State the preparation type.
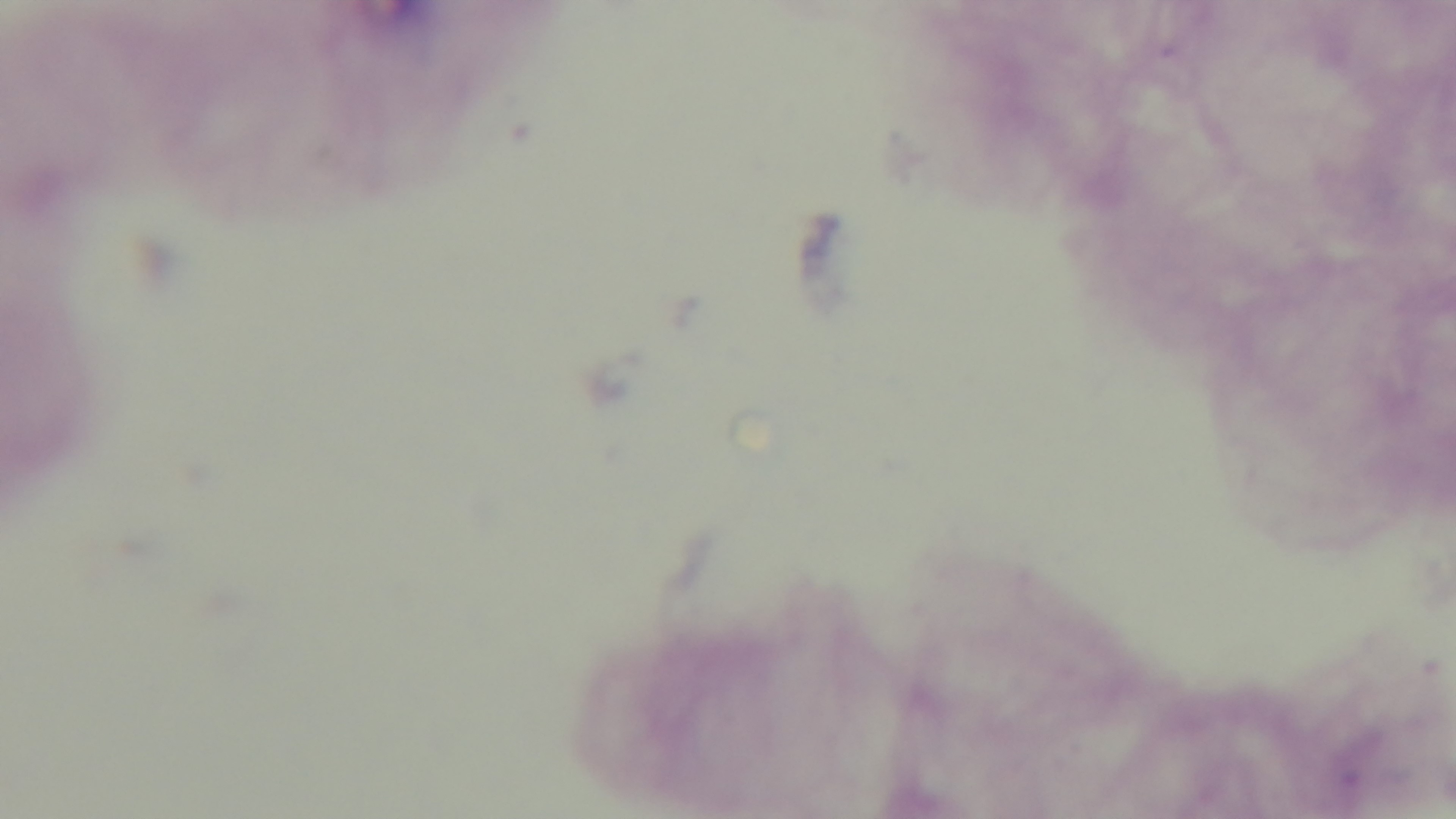
Thick.

stain = Giemsa
field of view = single
malaria status = negative
modality = light microscopy
capture = mounted 4K digital camera
objective = 100x oil immersion